Identify the blood parasite species.
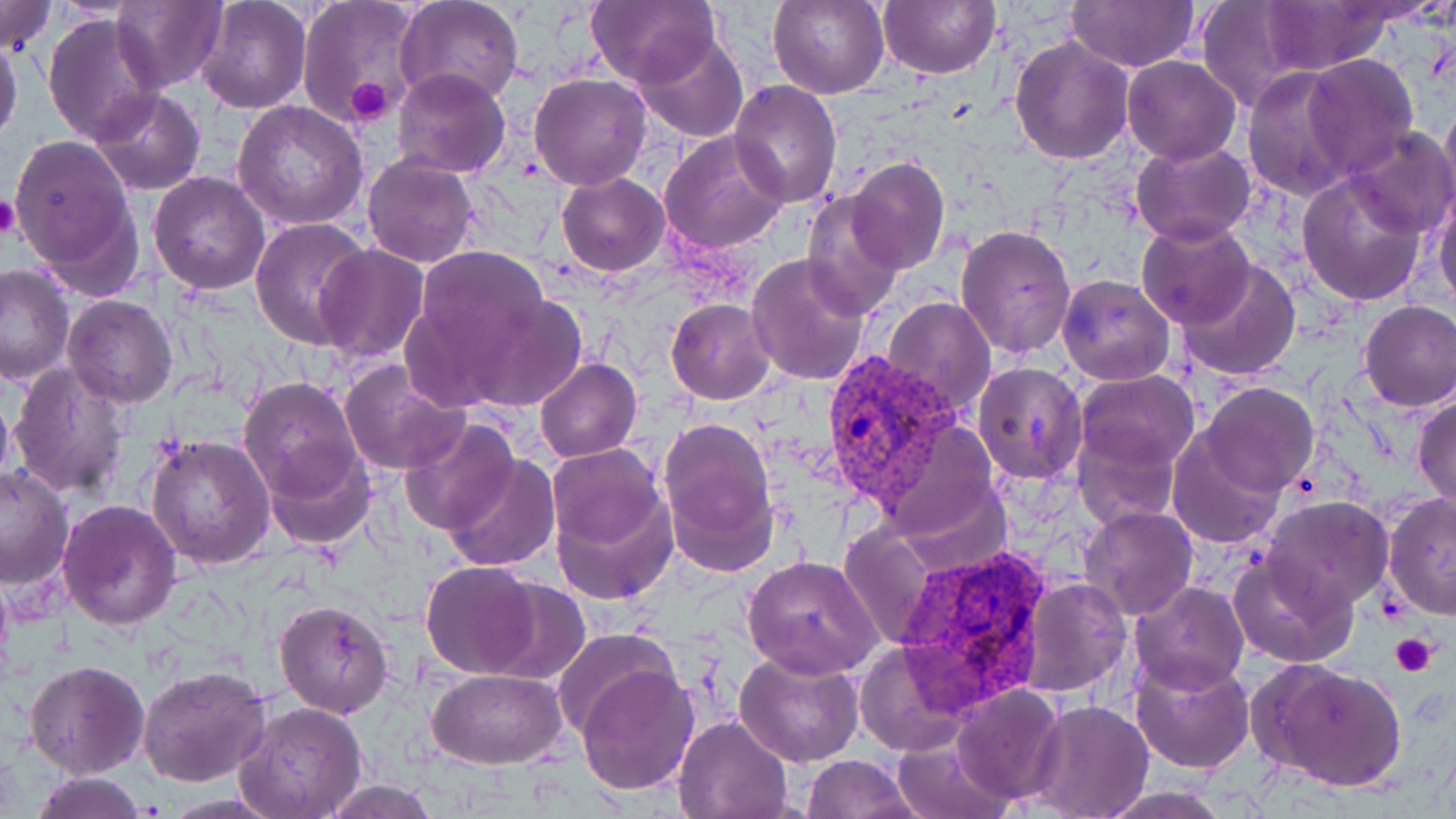

Plasmodium vivax.

Approximate bounding boxes as named x1/y1/x2/y2 corners in pixels. Uninfected red blood cell locations: (x1=0, y1=0, x2=55, y2=55), (x1=196, y1=0, x2=311, y2=113), (x1=769, y1=0, x2=891, y2=100), (x1=879, y1=0, x2=1000, y2=79), (x1=1066, y1=0, x2=1201, y2=71), (x1=1262, y1=0, x2=1394, y2=73), (x1=111, y1=1, x2=227, y2=92), (x1=394, y1=1, x2=524, y2=109), (x1=1197, y1=1, x2=1318, y2=111), (x1=297, y1=2, x2=425, y2=127), (x1=586, y1=2, x2=717, y2=88), (x1=43, y1=12, x2=163, y2=144), (x1=632, y1=31, x2=748, y2=143), (x1=1, y1=36, x2=24, y2=144), (x1=1010, y1=36, x2=1136, y2=165), (x1=1301, y1=53, x2=1419, y2=178), (x1=1122, y1=56, x2=1241, y2=165), (x1=1241, y1=66, x2=1359, y2=201), (x1=392, y1=68, x2=511, y2=178), (x1=530, y1=72, x2=651, y2=189), (x1=730, y1=79, x2=843, y2=209), (x1=90, y1=87, x2=206, y2=195), (x1=1439, y1=95, x2=1456, y2=221), (x1=233, y1=101, x2=368, y2=230), (x1=1345, y1=125, x2=1456, y2=239), (x1=659, y1=129, x2=788, y2=257), (x1=8, y1=136, x2=138, y2=284), (x1=1131, y1=140, x2=1255, y2=247), (x1=361, y1=155, x2=480, y2=268), (x1=845, y1=155, x2=951, y2=275), (x1=1296, y1=169, x2=1429, y2=305), (x1=150, y1=172, x2=271, y2=295), (x1=557, y1=173, x2=669, y2=275), (x1=1432, y1=182, x2=1456, y2=313), (x1=802, y1=191, x2=907, y2=319), (x1=249, y1=217, x2=372, y2=349), (x1=1135, y1=218, x2=1255, y2=330), (x1=954, y1=224, x2=1077, y2=360), (x1=314, y1=245, x2=430, y2=363), (x1=410, y1=246, x2=554, y2=368), (x1=747, y1=254, x2=871, y2=389), (x1=1176, y1=258, x2=1302, y2=380), (x1=0, y1=262, x2=76, y2=384), (x1=1057, y1=274, x2=1176, y2=385), (x1=461, y1=293, x2=587, y2=413), (x1=62, y1=294, x2=178, y2=406), (x1=884, y1=297, x2=997, y2=419), (x1=666, y1=299, x2=777, y2=404), (x1=1358, y1=300, x2=1455, y2=412), (x1=535, y1=357, x2=641, y2=463), (x1=340, y1=361, x2=473, y2=477), (x1=9, y1=362, x2=133, y2=500), (x1=972, y1=362, x2=1088, y2=484), (x1=1075, y1=369, x2=1200, y2=475), (x1=238, y1=377, x2=363, y2=500), (x1=0, y1=383, x2=16, y2=499), (x1=1201, y1=383, x2=1317, y2=497), (x1=1412, y1=392, x2=1456, y2=510), (x1=399, y1=415, x2=520, y2=536), (x1=659, y1=417, x2=778, y2=563), (x1=1074, y1=428, x2=1180, y2=525), (x1=1168, y1=429, x2=1287, y2=550), (x1=145, y1=435, x2=276, y2=571), (x1=262, y1=442, x2=376, y2=550), (x1=548, y1=444, x2=669, y2=560), (x1=443, y1=454, x2=559, y2=571), (x1=0, y1=464, x2=76, y2=589), (x1=550, y1=480, x2=680, y2=608), (x1=1384, y1=494, x2=1456, y2=619), (x1=1264, y1=498, x2=1394, y2=611), (x1=58, y1=500, x2=182, y2=631), (x1=1080, y1=504, x2=1197, y2=619), (x1=835, y1=521, x2=943, y2=649), (x1=1230, y1=553, x2=1357, y2=669), (x1=743, y1=556, x2=881, y2=677), (x1=421, y1=562, x2=542, y2=678), (x1=1018, y1=576, x2=1132, y2=696), (x1=483, y1=580, x2=592, y2=685), (x1=1127, y1=582, x2=1250, y2=696), (x1=275, y1=599, x2=392, y2=717), (x1=552, y1=628, x2=679, y2=742), (x1=854, y1=640, x2=976, y2=760), (x1=733, y1=647, x2=866, y2=768), (x1=1129, y1=654, x2=1256, y2=773), (x1=24, y1=658, x2=148, y2=777), (x1=1257, y1=661, x2=1405, y2=790), (x1=138, y1=663, x2=271, y2=787), (x1=576, y1=663, x2=700, y2=796), (x1=427, y1=667, x2=566, y2=768), (x1=953, y1=684, x2=1066, y2=804), (x1=1026, y1=699, x2=1154, y2=819), (x1=237, y1=701, x2=369, y2=819), (x1=674, y1=716, x2=794, y2=819), (x1=890, y1=736, x2=1014, y2=819), (x1=802, y1=754, x2=923, y2=819), (x1=25, y1=772, x2=150, y2=819), (x1=319, y1=778, x2=442, y2=818), (x1=1096, y1=786, x2=1235, y2=818). Platelet locations: (x1=346, y1=74, x2=397, y2=124), (x1=0, y1=196, x2=21, y2=242), (x1=1390, y1=633, x2=1438, y2=676). Plasmodium vivax-infected red blood cell locations: (x1=820, y1=349, x2=965, y2=510), (x1=892, y1=545, x2=1055, y2=710). Image is 1456×819 pixels. Single field of view. Thin blood film. May-Grünwald-Giemsa-stained preparation. Light microscopy. 1000x magnification.